Report the malaria status of this cell.
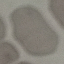

Uninfected.

{
  "preparation": "thin blood film",
  "image_type": "automatically extracted cell patch, resized to 64 × 64 pixels",
  "capture": "smartphone camera at the microscope eyepiece",
  "stain": "Giemsa"
}